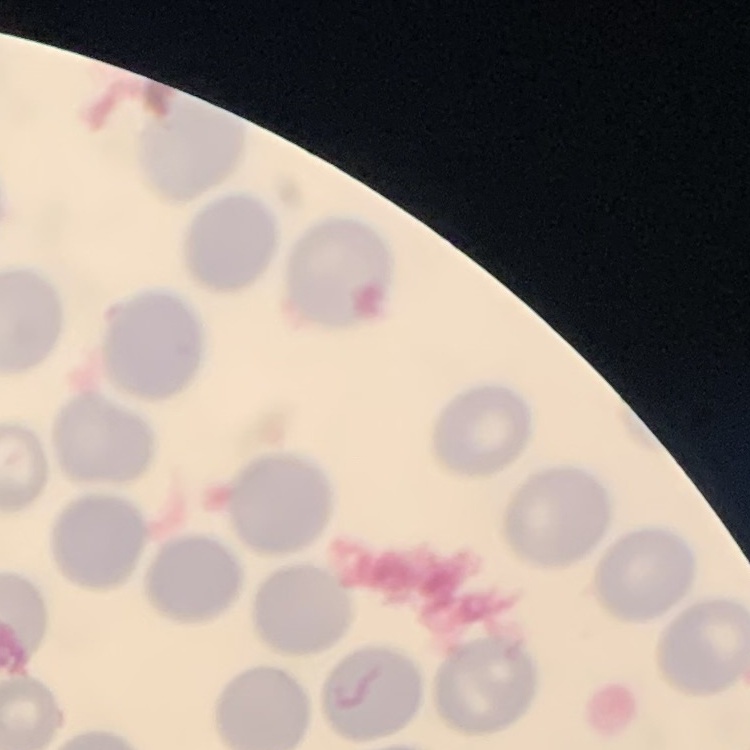
erythrocyte morphology = no rouleaux formation
image type = square crop of a larger photomicrograph
stain = Field's or Giemsa
preparation = thin blood film